Give the position of every malaria parasite, noting whether each is a trophozoite, schizont, or gametocyte.
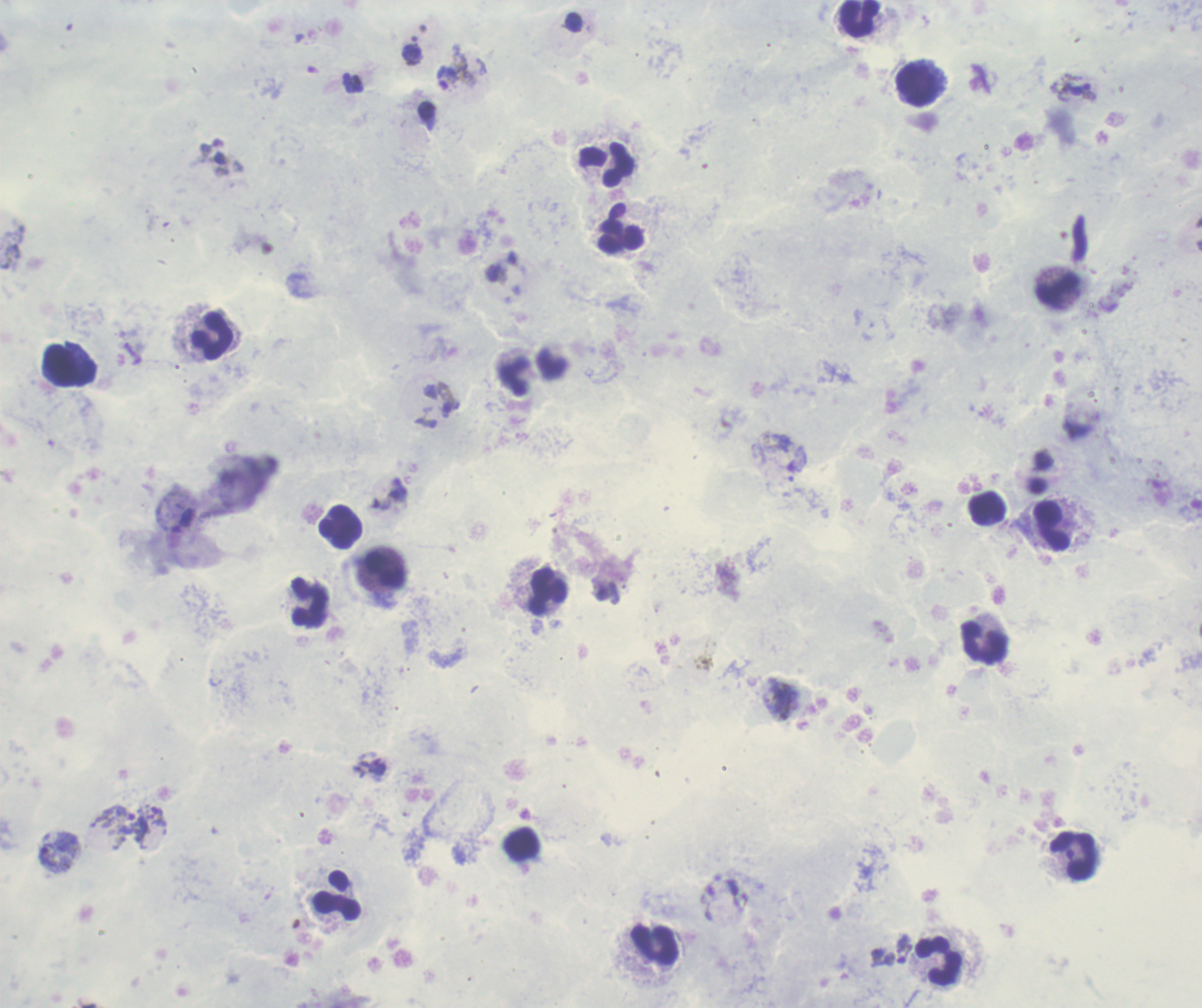

Approximate object centers, in pixels from the top-left corner.
Trophozoites: (x=447, y=78), (x=1073, y=92), (x=373, y=764), (x=905, y=949).
No schizont or gametocyte forms observed.

coordinate format = approximate object centers, in pixels from the top-left corner
leukocyte locations = (x=861, y=18), (x=919, y=85), (x=605, y=165), (x=622, y=228), (x=1056, y=291), (x=212, y=336), (x=69, y=365), (x=512, y=377), (x=987, y=509), (x=342, y=526), (x=1053, y=526), (x=385, y=571), (x=548, y=590), (x=309, y=602), (x=985, y=642), (x=1074, y=855), (x=337, y=896), (x=654, y=946), (x=938, y=961)
magnification = 100x
image size = 1202×1008 pixels
coloration quality = good
preparation = thick blood film
stain = Romanowsky
field of view = one from this slide
context = previously used in an actual diagnosis
background quality = poor